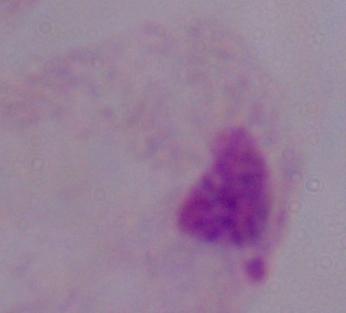

identification = trichomonad
magnification = 1000x
modality = micrograph